State which cell type is depicted.
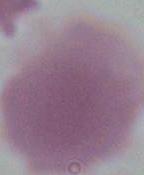
An erythrocyte.

Summary:
  - Modality: micrograph
  - Magnification: 1000x